Assess this cell for malaria.
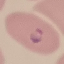

Parasitized.

Automatically extracted cell patch, resized to 64 × 64 pixels. Thin blood smear. Photographed with a smartphone camera at the microscope eyepiece. Giemsa stain.